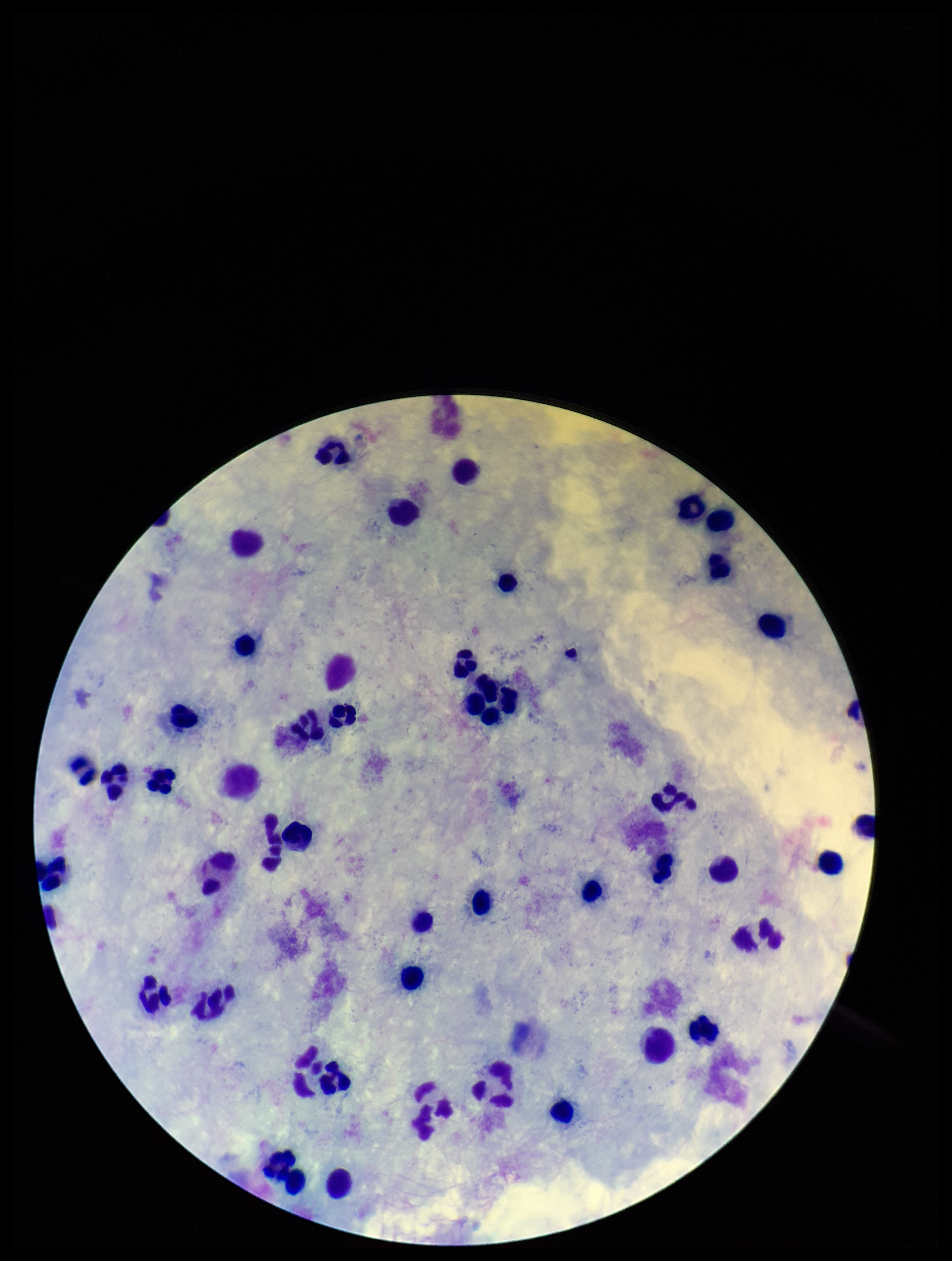

Summary:
  - Field of view: single
  - Stain: Giemsa
  - Parasite count: 0
  - Capture: smartphone photograph through the microscope eyepiece
  - Plasmodium parasites: none identified
  - Preparation: thick
  - Leukocyte count: 49
  - Image size: 952×1261 pixels
  - Patient malaria status: negative